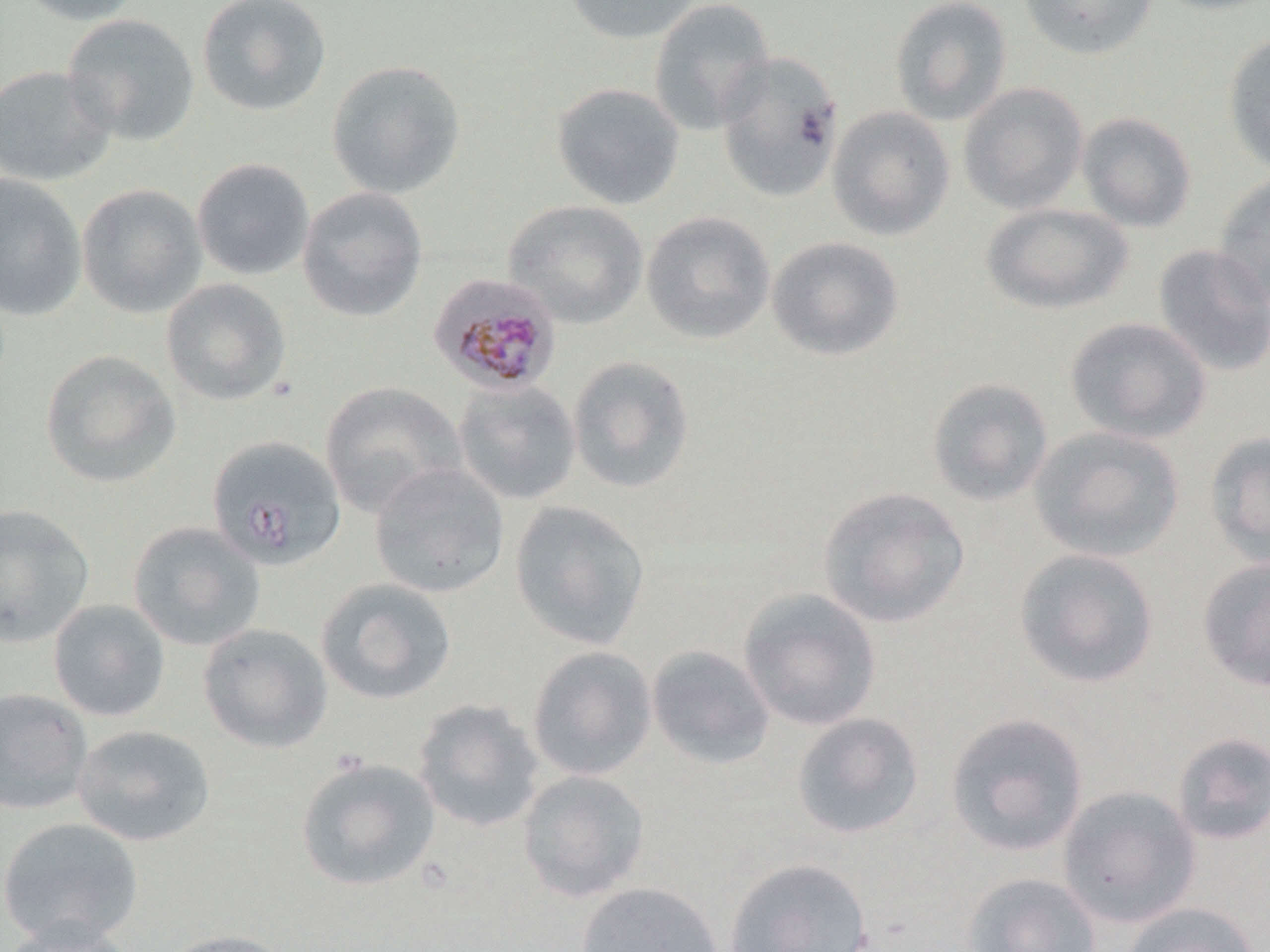

Summary:
  - Coordinate format: approximate bounding boxes as (x1,y1)-(x2,y2) corner pairs in pixels
  - Plasmodium malariae-infected red blood cell locations: (428,273)-(561,395)
  - Uninfected red blood cell locations: (13,0)-(149,25), (196,0)-(332,117), (563,0)-(702,44), (647,0)-(775,136), (889,0)-(1013,126), (1019,0)-(1158,60), (1146,0)-(1270,15), (61,14)-(200,146), (1222,32)-(1270,178), (714,51)-(844,202), (326,60)-(466,199), (0,65)-(117,187), (551,82)-(685,210), (958,82)-(1088,214), (826,106)-(955,241), (1077,111)-(1197,233), (191,158)-(315,281), (1213,172)-(1270,311), (0,173)-(87,322), (76,183)-(207,319), (296,186)-(429,323), (504,199)-(648,328), (980,203)-(1133,315), (641,211)-(775,345), (766,236)-(904,361), (1152,244)-(1270,377), (160,278)-(291,407), (1064,316)-(1212,444), (39,349)-(181,488), (567,356)-(695,494), (926,377)-(1054,506), (452,378)-(582,505), (319,381)-(465,517), (1029,426)-(1185,562), (1204,430)-(1270,567), (206,436)-(346,571), (369,463)-(509,598), (817,486)-(970,628), (509,500)-(650,650), (0,503)-(95,647), (127,521)-(265,651), (1013,548)-(1160,689), (1197,557)-(1270,691), (315,577)-(457,704), (737,588)-(882,731), (48,599)-(170,722), (197,622)-(333,753), (646,645)-(775,770), (527,646)-(657,780), (0,687)-(93,816), (413,698)-(545,833), (791,712)-(925,840), (944,712)-(1089,856), (72,724)-(216,847), (1171,732)-(1270,845), (295,756)-(441,891), (517,769)-(650,902), (1058,785)-(1202,928), (0,816)-(144,946), (723,857)-(873,951), (962,871)-(1102,952), (574,880)-(723,952), (1122,901)-(1262,952), (0,919)-(140,952), (156,928)-(296,952)
  - Slide-level diagnosis: Plasmodium malariae
  - Modality: light microscopy
  - Preparation: thin blood film
  - Stain: May-Grünwald-Giemsa
  - Field of view: one of a larger specimen
  - Magnification: 1000x
  - Image size: 1270×952 pixels